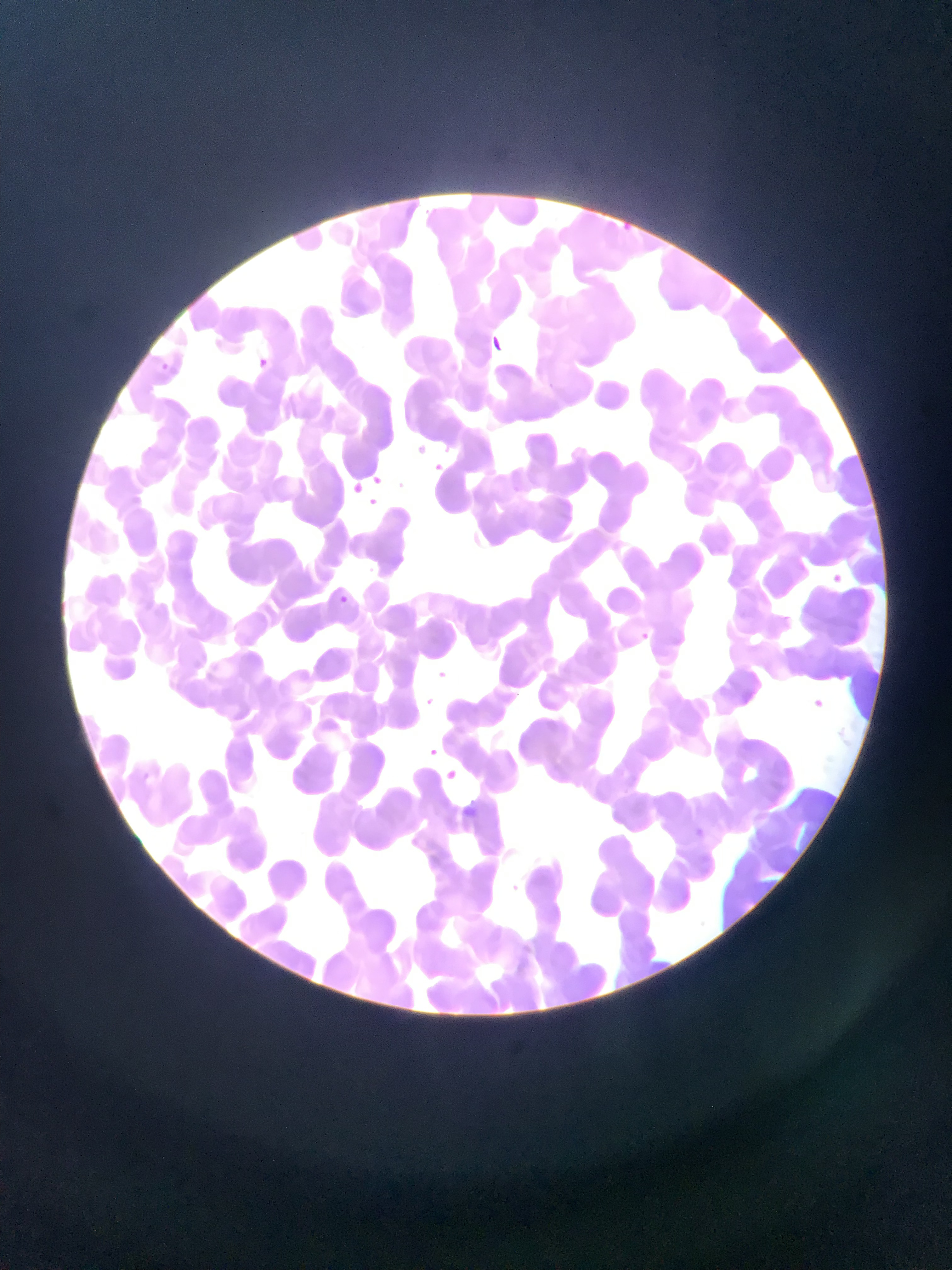
Approximate bounding boxes as [left, top, right, bottom] in pixels. Plasmodium parasite locations: [480, 331, 514, 362], [250, 351, 274, 375], [157, 354, 168, 382], [411, 434, 433, 451], [430, 461, 446, 473], [367, 467, 381, 493], [345, 477, 365, 494], [367, 493, 391, 510], [824, 569, 847, 590], [330, 589, 357, 612], [631, 628, 658, 652], [427, 662, 456, 690], [805, 691, 831, 715], [422, 743, 442, 761], [440, 764, 461, 785], [689, 823, 711, 844]. Sample from Ghana. Thin blood film. Photographed through a microscope with a mobile-phone camera. Single field of view. Image is 952×1270 pixels.